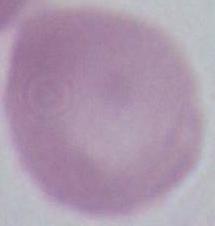

Captured at 1000x magnification. Photomicrograph. An erythrocyte is seen.